Report the malaria status of this cell.
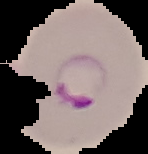
Parasitized.

preparation = thin blood smear
image type = segmented cell region with the area outside set to black
image size = 148×154 pixels